Locate every uninfected red blood cell.
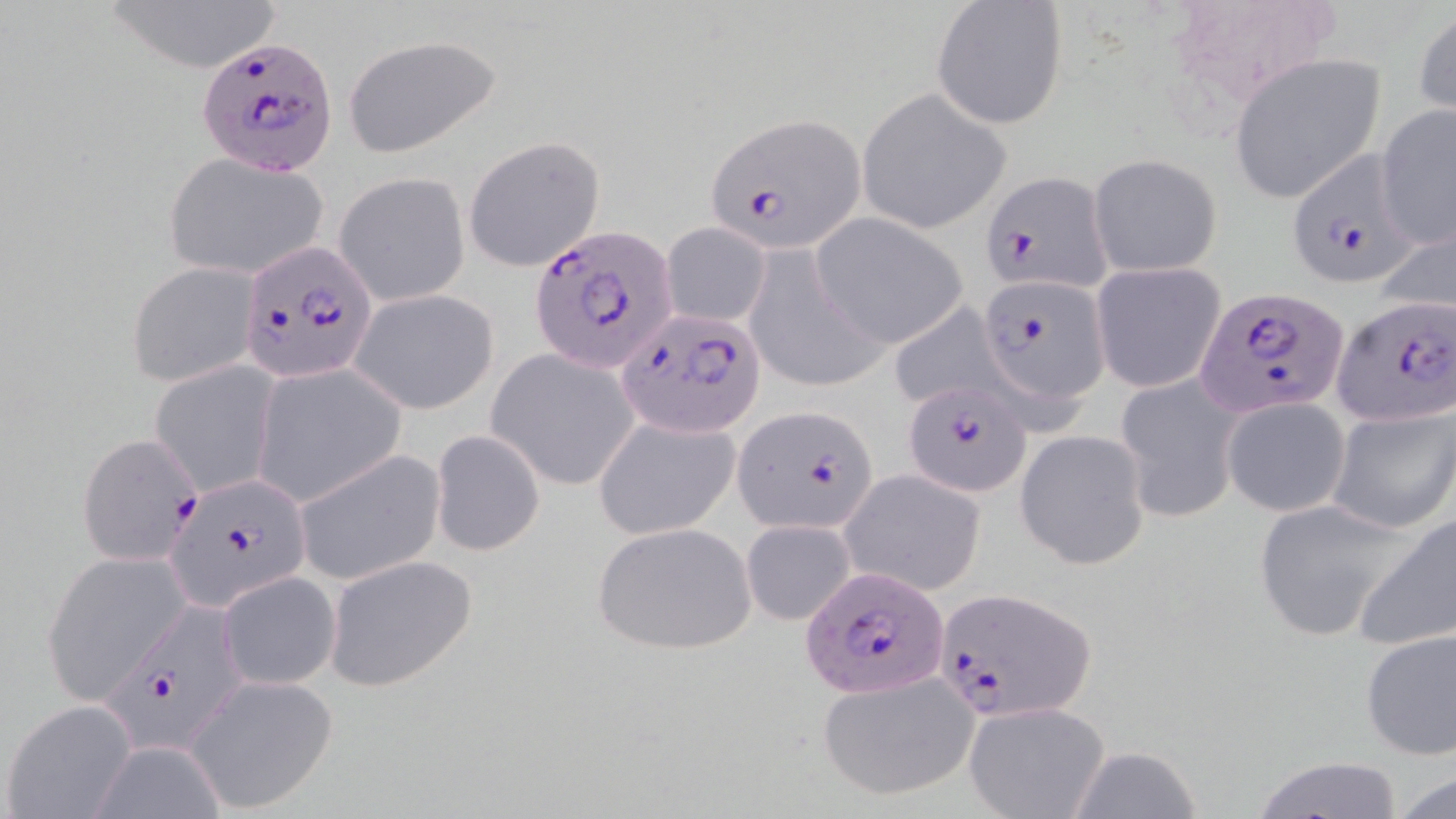
Approximate bounding boxes as [x1, y1, x2, y2] in pixels.
Uninfected red blood cells: [97, 0, 287, 70], [933, 1, 1069, 128], [1161, 1, 1340, 115], [1413, 8, 1456, 120], [341, 33, 504, 159], [1227, 52, 1388, 204], [856, 87, 1013, 235], [1376, 105, 1456, 251], [463, 135, 605, 272], [163, 152, 329, 280], [1089, 153, 1222, 277], [335, 172, 470, 306], [813, 216, 965, 348], [659, 221, 773, 329], [1376, 223, 1456, 317], [741, 246, 887, 392], [1090, 261, 1228, 395], [127, 262, 262, 388], [349, 288, 499, 413], [885, 300, 1011, 414], [486, 351, 639, 490], [149, 362, 278, 499], [253, 365, 403, 504], [1116, 373, 1244, 523], [1222, 396, 1350, 517], [1327, 403, 1456, 534], [591, 415, 741, 540], [431, 429, 545, 556], [1015, 429, 1152, 571], [294, 449, 445, 585], [841, 470, 987, 597], [1252, 499, 1418, 643], [1352, 511, 1456, 650], [740, 520, 857, 626], [590, 522, 757, 655], [43, 551, 190, 700], [323, 555, 478, 690], [219, 572, 341, 689], [1359, 627, 1456, 759], [816, 672, 978, 802], [184, 676, 338, 812], [2, 699, 139, 818], [964, 701, 1110, 819], [88, 739, 226, 819], [1064, 745, 1206, 819], [1248, 755, 1410, 818], [1386, 768, 1456, 818].

Plasmodium falciparum-infected red blood cell locations: [196, 38, 339, 176], [707, 113, 868, 251], [1285, 149, 1420, 291], [979, 170, 1114, 295], [529, 224, 675, 374], [240, 243, 375, 379], [978, 274, 1109, 411], [1198, 287, 1350, 420], [1333, 296, 1455, 428], [616, 310, 767, 439], [902, 378, 1030, 497], [734, 404, 879, 535], [78, 434, 204, 567], [168, 473, 309, 609], [801, 565, 950, 702], [933, 587, 1097, 723], [99, 604, 251, 755]. Slide-level diagnosis: Plasmodium falciparum. Thin blood film. Light microscopy. Captured at 1000x magnification. May-Grünwald-Giemsa-stained preparation. One field of a larger specimen. Image is 1456×819 pixels.